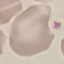
Malaria status: uninfected. Giemsa stain. Thin blood film. Automatically extracted cell patch, resized to 64 × 64 pixels. Photographed with a smartphone camera at the microscope eyepiece.